Classify this cell by malaria status.
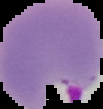

Parasitized.

image type = segmented cell region with the area outside set to black
image size = 103×109 pixels
preparation = thin blood smear